Find the red blood cells and label each as Plasmodium falciparum-infected, uninfected, or of indeterminate infection status.
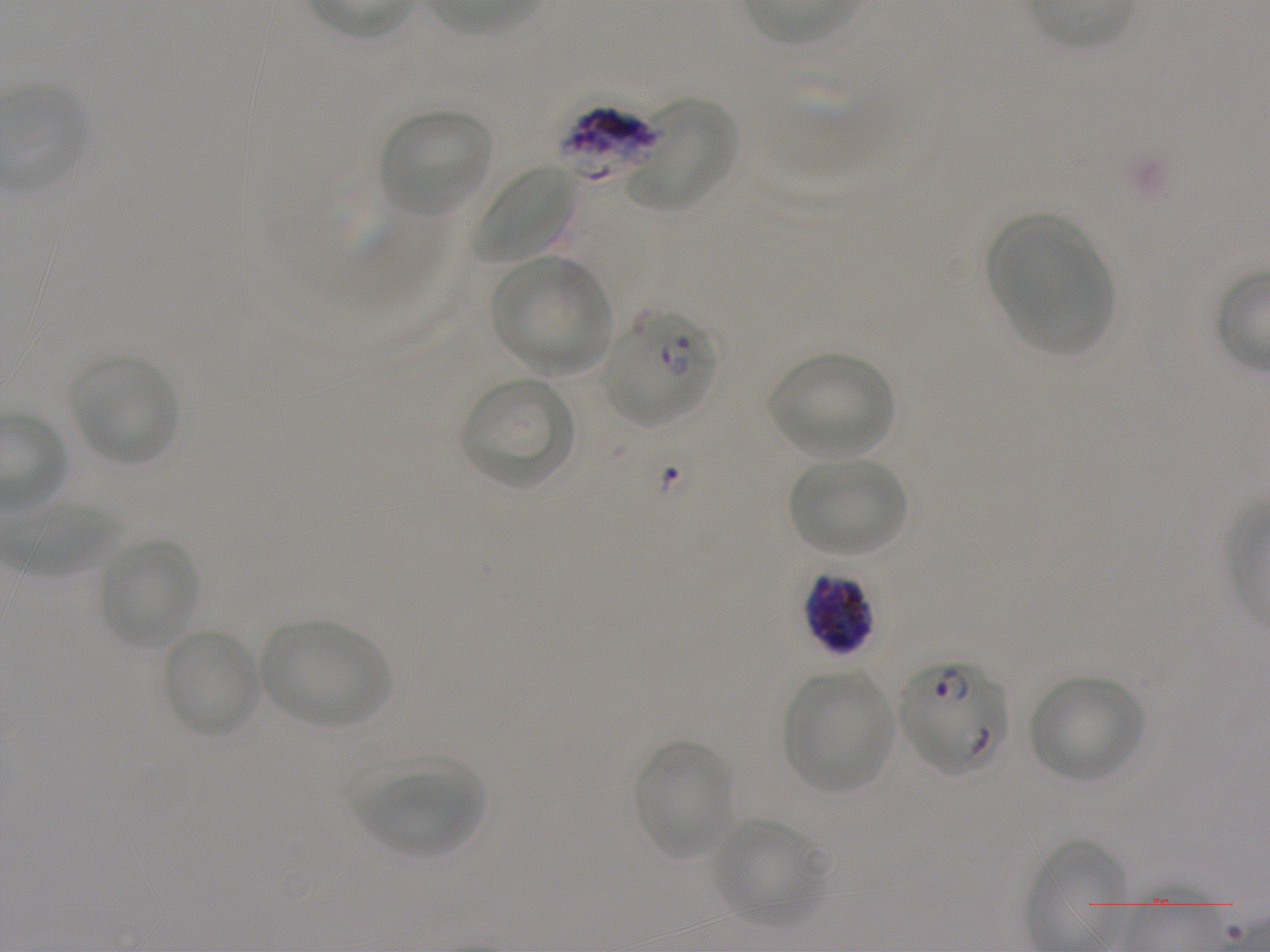
Approximate bounding boxes as {x1, y1, x2, y2} in pixels. Not every red blood cell is marked. A life-cycle stage — or a range of stages, where the recorded stages span more than one — follows each staged infected red blood cell.
Infected red blood cells: {604, 309, 718, 427} early ring to early schizont; {803, 572, 874, 656}; {899, 660, 1008, 776}.
Red blood cells of indeterminate infection status: {558, 105, 663, 179}.
Uninfected red blood cells: {627, 99, 735, 212}, {381, 109, 492, 217}, {473, 165, 578, 264}, {991, 218, 1111, 354}, {490, 256, 612, 375}, {769, 354, 893, 458}, {71, 358, 178, 466}, {460, 377, 575, 489}, {788, 458, 907, 556}, {100, 536, 198, 651}, {261, 620, 390, 728}, {163, 629, 260, 738}, {783, 671, 893, 792}, {1028, 676, 1145, 783}, {633, 740, 733, 859}, {352, 758, 485, 857}, {710, 817, 827, 925}.

Summary:
  - Preparation: thin blood film
  - Culture: in-vitro Plasmodium falciparum strain NF54, static
  - Stain: Giemsa
  - Objective: 100x, oil immersion, numerical aperture 1.25
  - Donor blood group: A+
  - Image size: 1270×952 pixels
  - Field of view: one from this slide